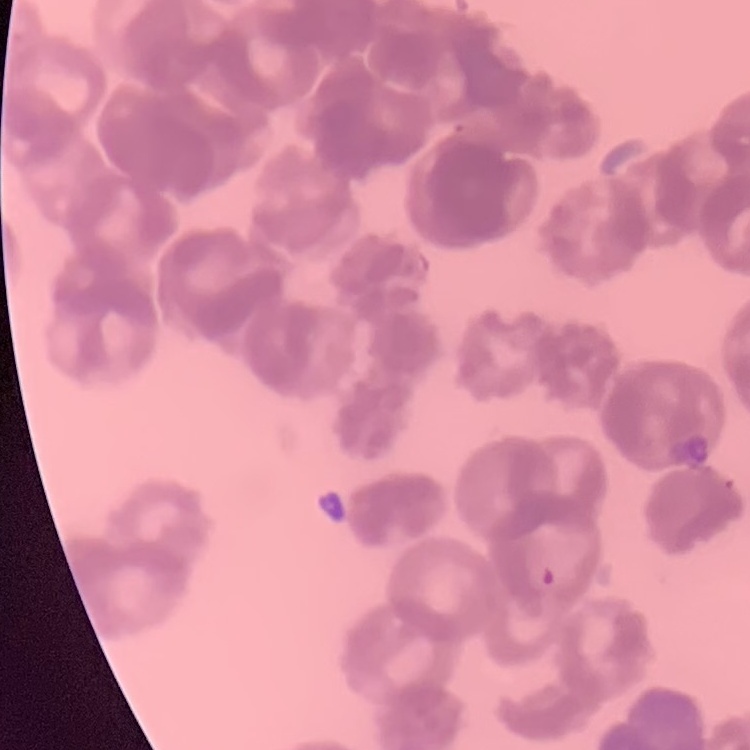 The red blood cells exhibit rouleaux formation. One tile cut from a larger photomicrograph. Thin blood film. Field's or Giemsa stain.